Classify this cell by malaria status.
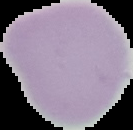
It is uninfected.

Summary:
  - Image type: cell region segmented out of the field of view; surrounding area masked to black
  - Image size: 133×130 pixels
  - Preparation: thin blood smear